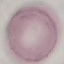
malaria status = uninfected
preparation = thin blood film
stain = Giemsa
capture = smartphone camera at the microscope eyepiece
image type = automatically extracted cell patch, resized to 64 × 64 pixels